Identify the blood parasite species.
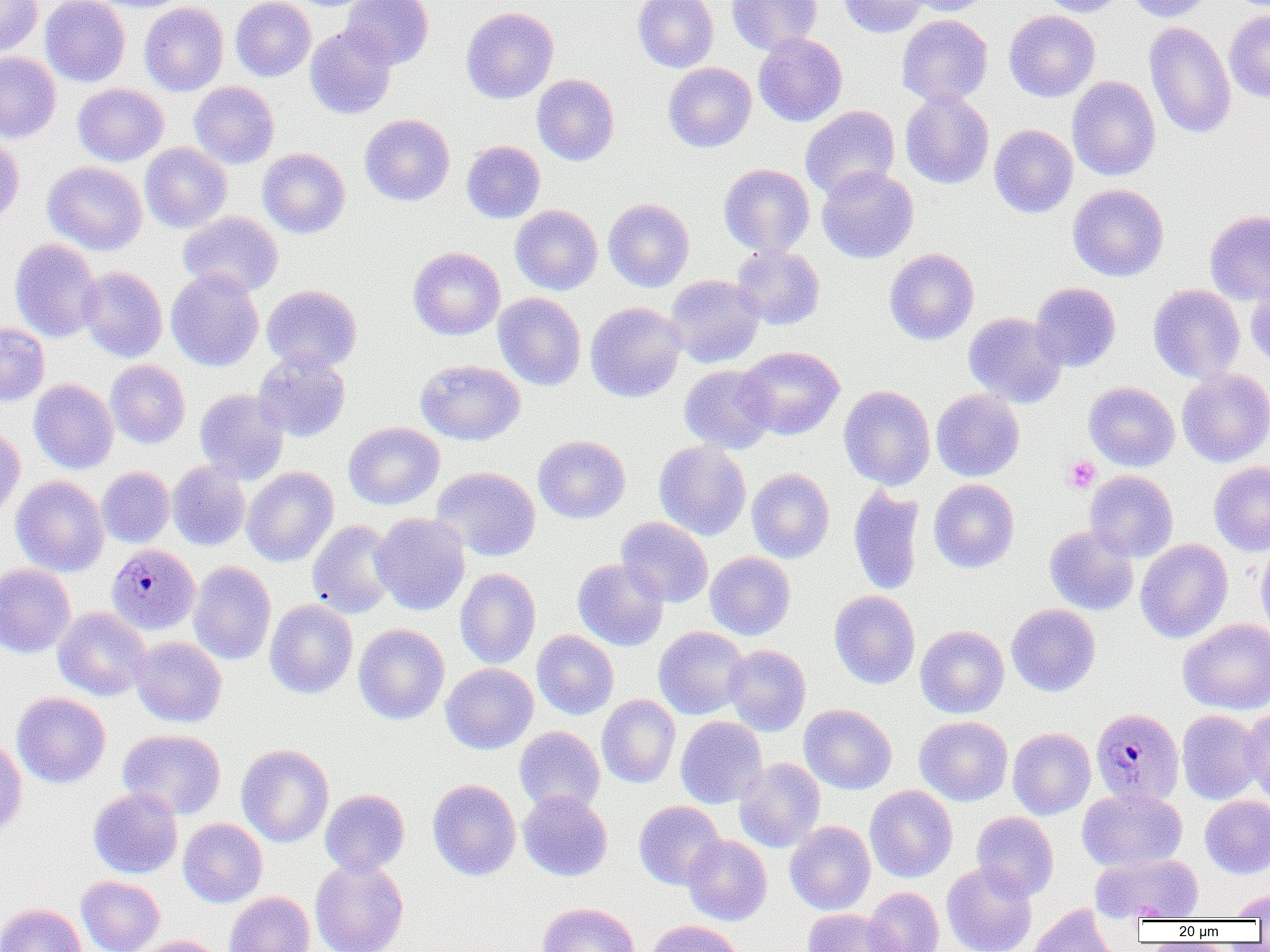
Plasmodium malariae.

image size = 1270×952 pixels
field of view = one of a larger specimen
magnification = 1000x
platelet locations = approximate bounding boxes as named x1/y1/x2/y2 corners in pixels: (x1=1063, y1=456, x2=1100, y2=493)
uninfected red blood cell locations = approximate bounding boxes as named x1/y1/x2/y2 corners in pixels: (x1=0, y1=0, x2=42, y2=58), (x1=40, y1=0, x2=130, y2=87), (x1=84, y1=0, x2=194, y2=12), (x1=231, y1=0, x2=315, y2=81), (x1=341, y1=0, x2=434, y2=69), (x1=632, y1=0, x2=719, y2=72), (x1=727, y1=0, x2=822, y2=55), (x1=837, y1=0, x2=930, y2=38), (x1=899, y1=0, x2=993, y2=17), (x1=1039, y1=0, x2=1129, y2=17), (x1=1126, y1=0, x2=1216, y2=22), (x1=139, y1=2, x2=228, y2=96), (x1=461, y1=6, x2=559, y2=104), (x1=1003, y1=10, x2=1100, y2=102), (x1=1224, y1=10, x2=1270, y2=102), (x1=896, y1=14, x2=993, y2=106), (x1=1144, y1=22, x2=1236, y2=139), (x1=305, y1=24, x2=398, y2=119), (x1=753, y1=33, x2=848, y2=127), (x1=0, y1=53, x2=61, y2=142), (x1=663, y1=62, x2=757, y2=152), (x1=531, y1=74, x2=619, y2=165), (x1=1066, y1=75, x2=1160, y2=181), (x1=189, y1=81, x2=279, y2=169), (x1=72, y1=83, x2=169, y2=166), (x1=900, y1=90, x2=994, y2=189), (x1=800, y1=105, x2=900, y2=200), (x1=360, y1=114, x2=455, y2=205), (x1=989, y1=124, x2=1078, y2=218), (x1=0, y1=134, x2=24, y2=226), (x1=462, y1=140, x2=545, y2=223), (x1=140, y1=142, x2=231, y2=233), (x1=258, y1=148, x2=350, y2=238), (x1=43, y1=161, x2=147, y2=255), (x1=718, y1=164, x2=815, y2=257), (x1=817, y1=166, x2=919, y2=263), (x1=1067, y1=184, x2=1169, y2=282), (x1=603, y1=198, x2=694, y2=292), (x1=510, y1=205, x2=602, y2=295), (x1=178, y1=211, x2=283, y2=298), (x1=1204, y1=211, x2=1270, y2=305), (x1=10, y1=238, x2=103, y2=342), (x1=731, y1=245, x2=825, y2=330), (x1=408, y1=246, x2=505, y2=340), (x1=884, y1=248, x2=979, y2=345), (x1=79, y1=267, x2=167, y2=363), (x1=166, y1=268, x2=264, y2=371), (x1=665, y1=275, x2=765, y2=368), (x1=1246, y1=277, x2=1270, y2=372), (x1=1030, y1=282, x2=1121, y2=372), (x1=1148, y1=284, x2=1245, y2=383), (x1=262, y1=285, x2=362, y2=372), (x1=493, y1=293, x2=586, y2=391), (x1=585, y1=302, x2=687, y2=402), (x1=963, y1=312, x2=1067, y2=407), (x1=0, y1=323, x2=49, y2=406), (x1=738, y1=346, x2=845, y2=440), (x1=253, y1=350, x2=351, y2=442), (x1=416, y1=359, x2=526, y2=445), (x1=105, y1=360, x2=190, y2=449), (x1=679, y1=364, x2=777, y2=454), (x1=1177, y1=368, x2=1270, y2=467), (x1=29, y1=379, x2=118, y2=474), (x1=1083, y1=381, x2=1180, y2=472), (x1=839, y1=385, x2=936, y2=489), (x1=194, y1=389, x2=289, y2=484), (x1=931, y1=389, x2=1024, y2=481), (x1=344, y1=421, x2=444, y2=509), (x1=0, y1=426, x2=25, y2=521), (x1=533, y1=435, x2=630, y2=523), (x1=653, y1=440, x2=751, y2=540), (x1=167, y1=460, x2=250, y2=550), (x1=1209, y1=461, x2=1270, y2=556), (x1=431, y1=466, x2=541, y2=561), (x1=96, y1=467, x2=175, y2=548), (x1=242, y1=467, x2=339, y2=567), (x1=746, y1=468, x2=835, y2=563), (x1=1084, y1=470, x2=1178, y2=562), (x1=11, y1=476, x2=109, y2=577), (x1=929, y1=479, x2=1019, y2=573), (x1=848, y1=485, x2=924, y2=596), (x1=848, y1=486, x2=1013, y2=589), (x1=371, y1=512, x2=471, y2=615), (x1=616, y1=517, x2=713, y2=608), (x1=306, y1=520, x2=399, y2=619), (x1=1044, y1=525, x2=1139, y2=616), (x1=1255, y1=538, x2=1270, y2=637), (x1=1135, y1=539, x2=1233, y2=643), (x1=705, y1=551, x2=796, y2=640), (x1=572, y1=558, x2=669, y2=651), (x1=188, y1=561, x2=276, y2=664), (x1=0, y1=563, x2=76, y2=658), (x1=455, y1=568, x2=541, y2=669), (x1=829, y1=590, x2=920, y2=689), (x1=264, y1=599, x2=358, y2=698), (x1=1006, y1=604, x2=1101, y2=696), (x1=53, y1=607, x2=151, y2=701), (x1=1179, y1=618, x2=1270, y2=714), (x1=353, y1=623, x2=450, y2=724), (x1=915, y1=625, x2=1009, y2=718), (x1=653, y1=626, x2=750, y2=719), (x1=532, y1=630, x2=619, y2=720), (x1=130, y1=636, x2=227, y2=727), (x1=723, y1=644, x2=811, y2=736), (x1=440, y1=662, x2=538, y2=754), (x1=11, y1=692, x2=110, y2=788), (x1=597, y1=694, x2=681, y2=788), (x1=799, y1=704, x2=897, y2=794), (x1=1239, y1=706, x2=1270, y2=802), (x1=1177, y1=710, x2=1264, y2=805), (x1=676, y1=716, x2=767, y2=808), (x1=914, y1=716, x2=1012, y2=806), (x1=514, y1=726, x2=604, y2=813), (x1=1007, y1=727, x2=1096, y2=819), (x1=118, y1=729, x2=226, y2=819), (x1=0, y1=736, x2=27, y2=839), (x1=236, y1=744, x2=334, y2=847), (x1=735, y1=758, x2=825, y2=852), (x1=427, y1=779, x2=521, y2=880), (x1=864, y1=785, x2=957, y2=882), (x1=88, y1=787, x2=183, y2=879), (x1=1077, y1=788, x2=1187, y2=871), (x1=320, y1=789, x2=410, y2=877), (x1=518, y1=789, x2=613, y2=881), (x1=1200, y1=795, x2=1270, y2=879), (x1=634, y1=800, x2=725, y2=890), (x1=971, y1=811, x2=1059, y2=901), (x1=178, y1=818, x2=267, y2=907), (x1=785, y1=821, x2=875, y2=915), (x1=682, y1=834, x2=772, y2=926), (x1=1091, y1=853, x2=1203, y2=921), (x1=310, y1=858, x2=408, y2=952), (x1=941, y1=861, x2=1038, y2=952), (x1=76, y1=876, x2=164, y2=952), (x1=864, y1=887, x2=944, y2=952), (x1=1229, y1=888, x2=1270, y2=920), (x1=224, y1=891, x2=315, y2=952), (x1=538, y1=902, x2=640, y2=952), (x1=0, y1=903, x2=86, y2=952), (x1=1026, y1=904, x2=1120, y2=952), (x1=802, y1=907, x2=902, y2=952), (x1=645, y1=919, x2=745, y2=952), (x1=135, y1=935, x2=223, y2=952)
Plasmodium malariae-infected red blood cell locations = approximate bounding boxes as named x1/y1/x2/y2 corners in pixels: (x1=107, y1=543, x2=200, y2=635), (x1=1091, y1=707, x2=1184, y2=806)
preparation = thin blood smear
modality = light microscopy